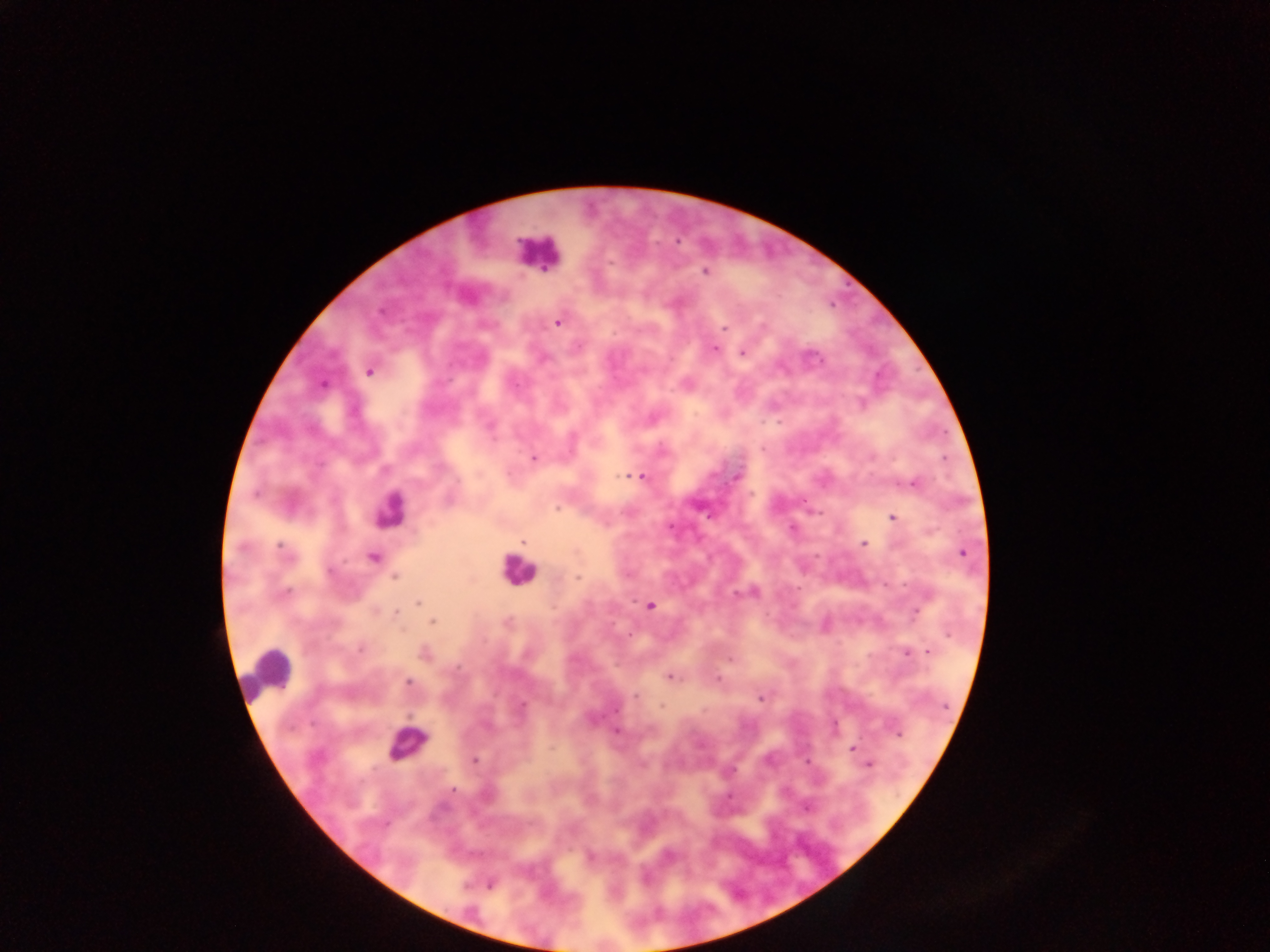
{
  "country": "Ghana",
  "malaria_parasite_locations": "approximate centers as {x, y} in pixels: {705, 272}, {557, 323}, {723, 327}, {715, 349}, {742, 353}, {545, 358}, {369, 371}, {323, 384}, {534, 458}, {631, 476}, {736, 476}, {642, 477}, {913, 484}, {558, 508}, {893, 517}, {670, 526}, {523, 542}, {863, 543}, {241, 547}, {282, 551}, {963, 553}, {372, 557}, {328, 571}, {395, 577}, {577, 577}, {736, 593}, {286, 594}, {417, 603}, {650, 606}, {397, 612}, {918, 612}, {433, 622}, {360, 649}, {929, 652}, {424, 654}, {906, 654}, {574, 659}, {669, 677}, {717, 679}, {408, 683}, {635, 697}, {761, 699}, {522, 705}, {661, 706}, {615, 710}, {617, 731}, {897, 733}, {852, 747}, {474, 761}, {870, 764}, {453, 789}, {729, 796}, {807, 807}, {590, 857}, {490, 884}",
  "capture": "mobile-phone photograph through a microscope",
  "field_of_view": "single",
  "preparation": "thick blood smear",
  "image_size": "1270×952 pixels",
  "leukocyte_locations": "approximate centers as {x, y} in pixels: {538, 253}, {389, 509}, {517, 570}, {268, 673}, {407, 744}"
}